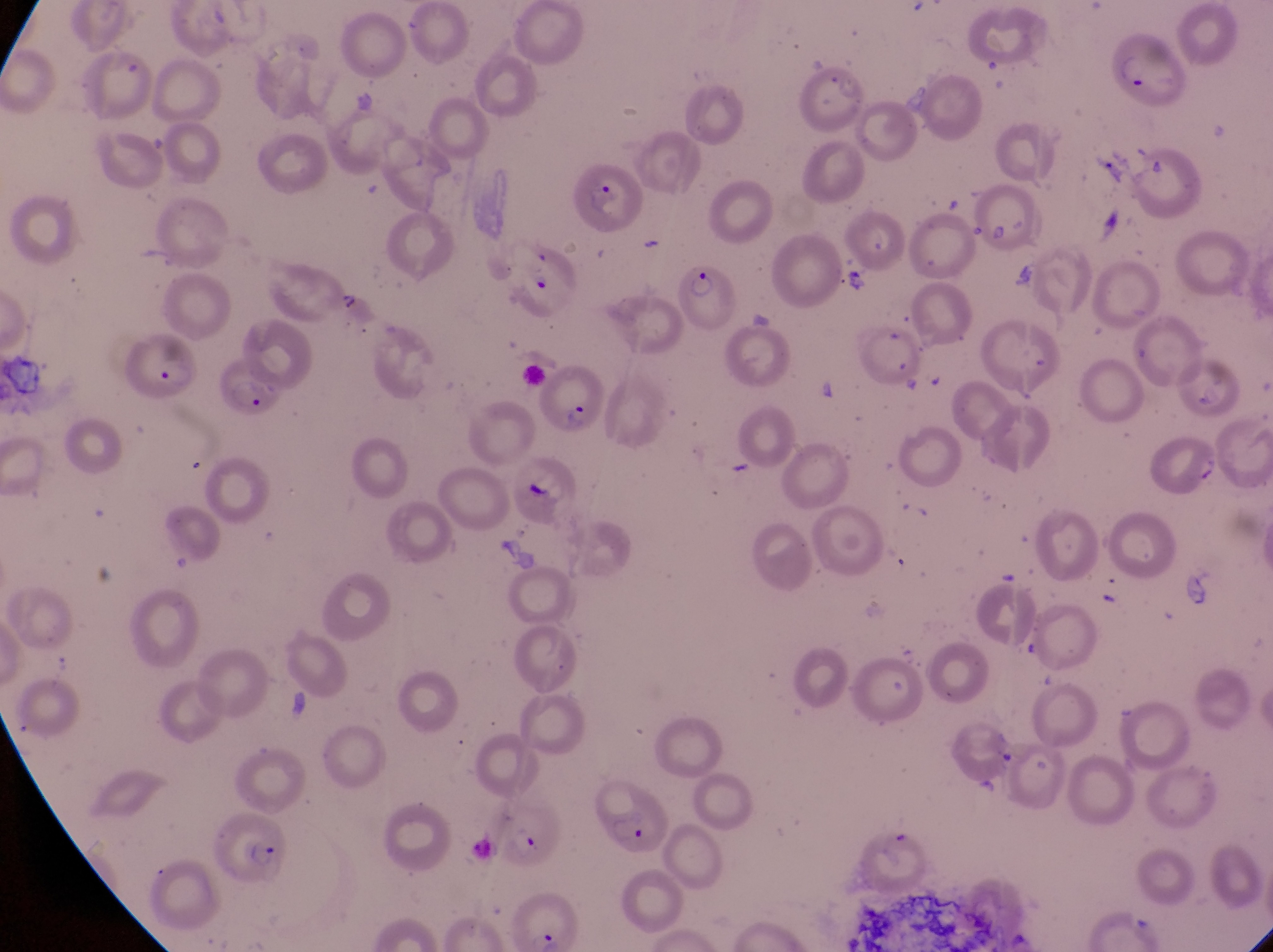
{
  "artifact_platelet_like_body_stain_precipitate_or_debris_locations": "approximate bounding boxes as (left, top, right, bottom) in pixels: (1093, 202, 1130, 247), (1008, 259, 1045, 292), (843, 264, 880, 297), (336, 290, 363, 319), (743, 302, 780, 334), (522, 477, 557, 512), (993, 741, 1021, 781)",
  "trophozoite_locations": "approximate bounding boxes as (left, top, right, bottom) in pixels: (527, 272, 555, 299)",
  "country": "Uganda",
  "preparation": "thin blood smear",
  "image_size": "1273×952 pixels",
  "field_of_view": "single",
  "capture": "smartphone photograph through the eyepiece of an Olympus CX-23 microscope",
  "parasitised_red_blood_cell_locations": "approximate bounding boxes as (left, top, right, bottom) in pixels: (579, 169, 651, 243), (973, 182, 1043, 247), (676, 257, 739, 331), (117, 339, 197, 401), (207, 352, 279, 422), (530, 364, 605, 436), (596, 784, 671, 856), (489, 802, 564, 869), (210, 814, 285, 877), (509, 900, 578, 952)",
  "magnification": "1000x"
}